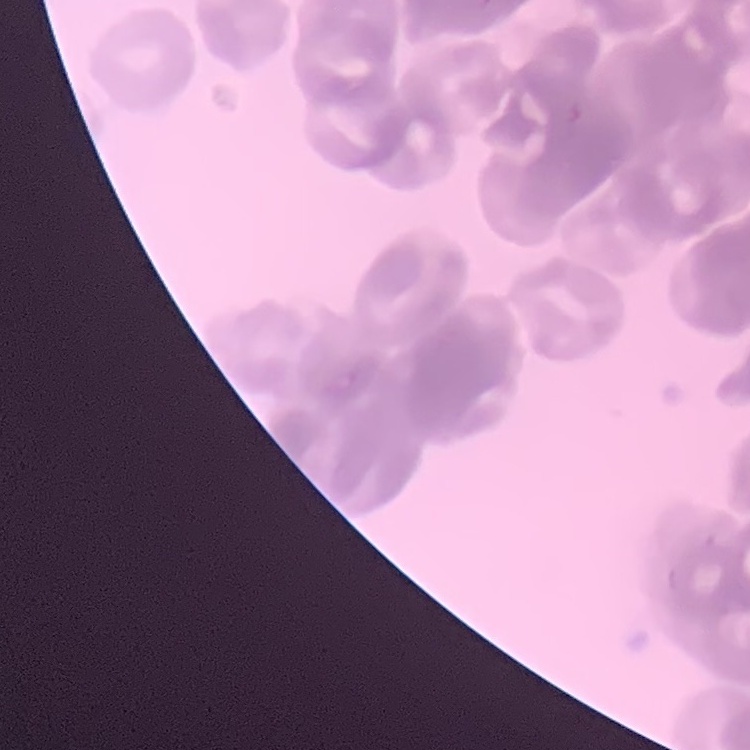
Summary:
  - Red blood cell morphology: rouleaux formation
  - Image type: square crop of a larger photomicrograph
  - Preparation: thin peripheral smear
  - Stain: Field's or Giemsa